Outline each Plasmodium falciparum parasite and classify it by life-cycle stage.
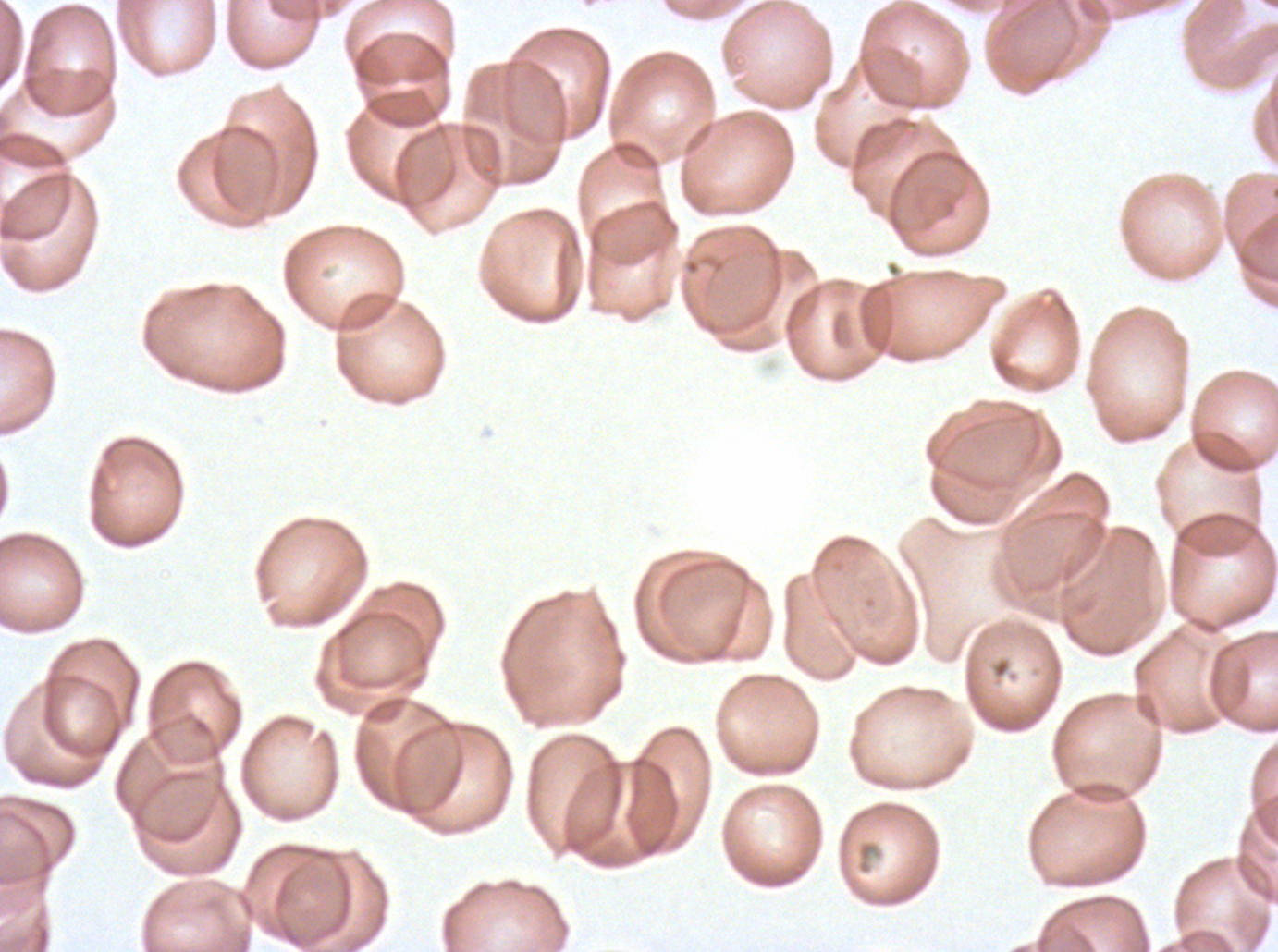
No rings, late-ring/early-trophozoite forms, mid trophozoites, late trophozoites, early schizonts, late schizonts, segmenters, or gametocytes observed.

Approximate bounding boxes as {x1, y1, x2, y2} in pixels.
Summary:
  - Debris locations: {857, 841, 876, 861}
  - Stain: Giemsa
  - Image size: 1278×952 pixels
  - Preparation: thin blood smear
  - Field of view: sub-image separated from a larger composite
  - Specimen: ex-vivo Plasmodium falciparum culture from a patient in The Gambia, grown for 24 to 48 hours